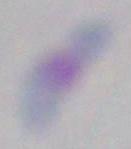

modality: micrograph
identification: Toxoplasma gondii
magnification: 1000x